Describe the morphology of the red blood cells.
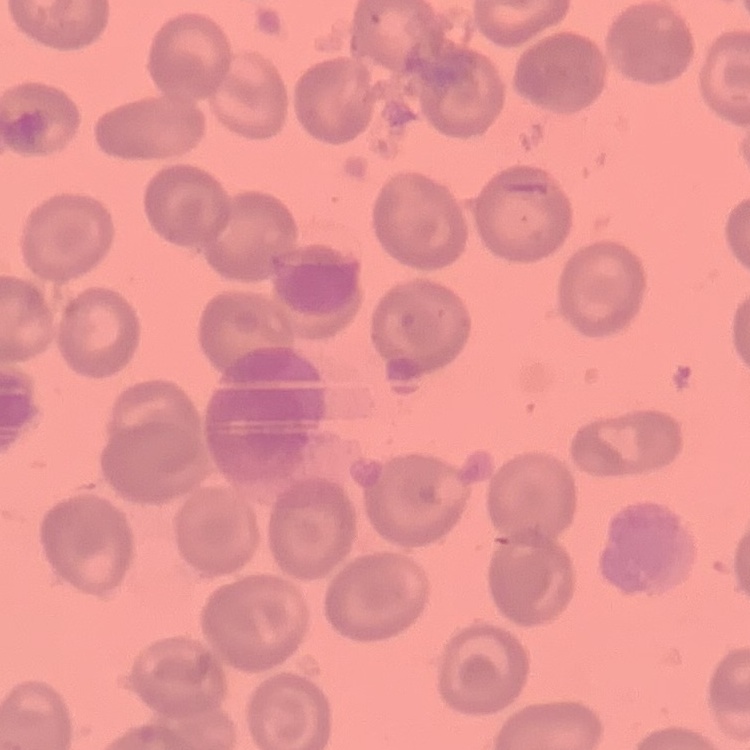

No rouleaux formation.

Summary:
  - Preparation: thin peripheral smear
  - Image type: square crop of a larger photomicrograph
  - Stain: Field's or Giemsa